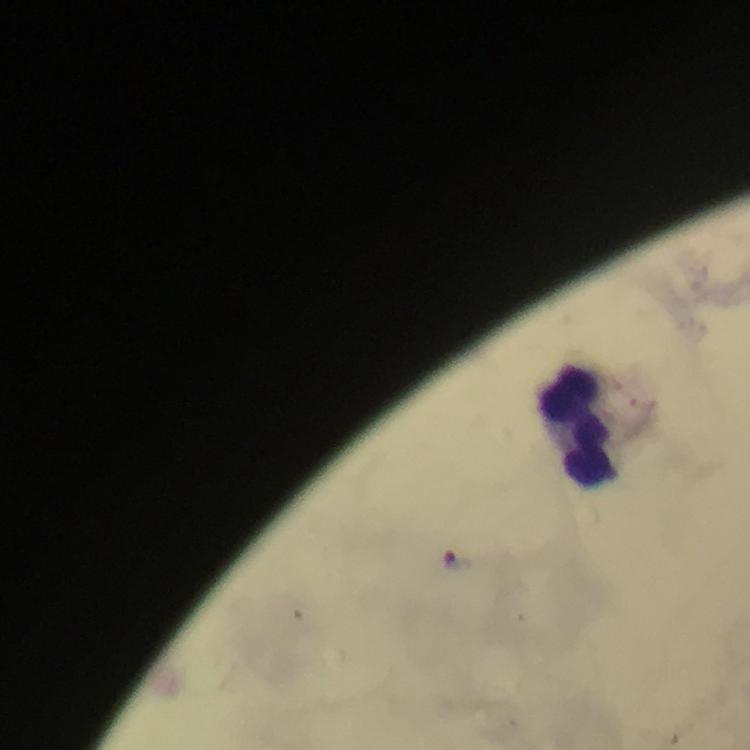
Approximate object centers, in pixels from the top-left corner. Leukocyte locations: (x=587, y=426). Photographed with a smartphone mounted on the microscope. Giemsa stain. 100x magnification. Thick smear. Plasmodium parasites: none detected. Immersion oil was used. Image is 750×750 pixels. A crop from one field of view. From a diagnostic examination for malaria.